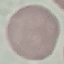

Summary:
  - Malaria status: uninfected
  - Stain: Giemsa
  - Preparation: thin smear
  - Capture: smartphone through the microscope eyepiece
  - Image type: automatically extracted cell patch, resized to 64 × 64 pixels